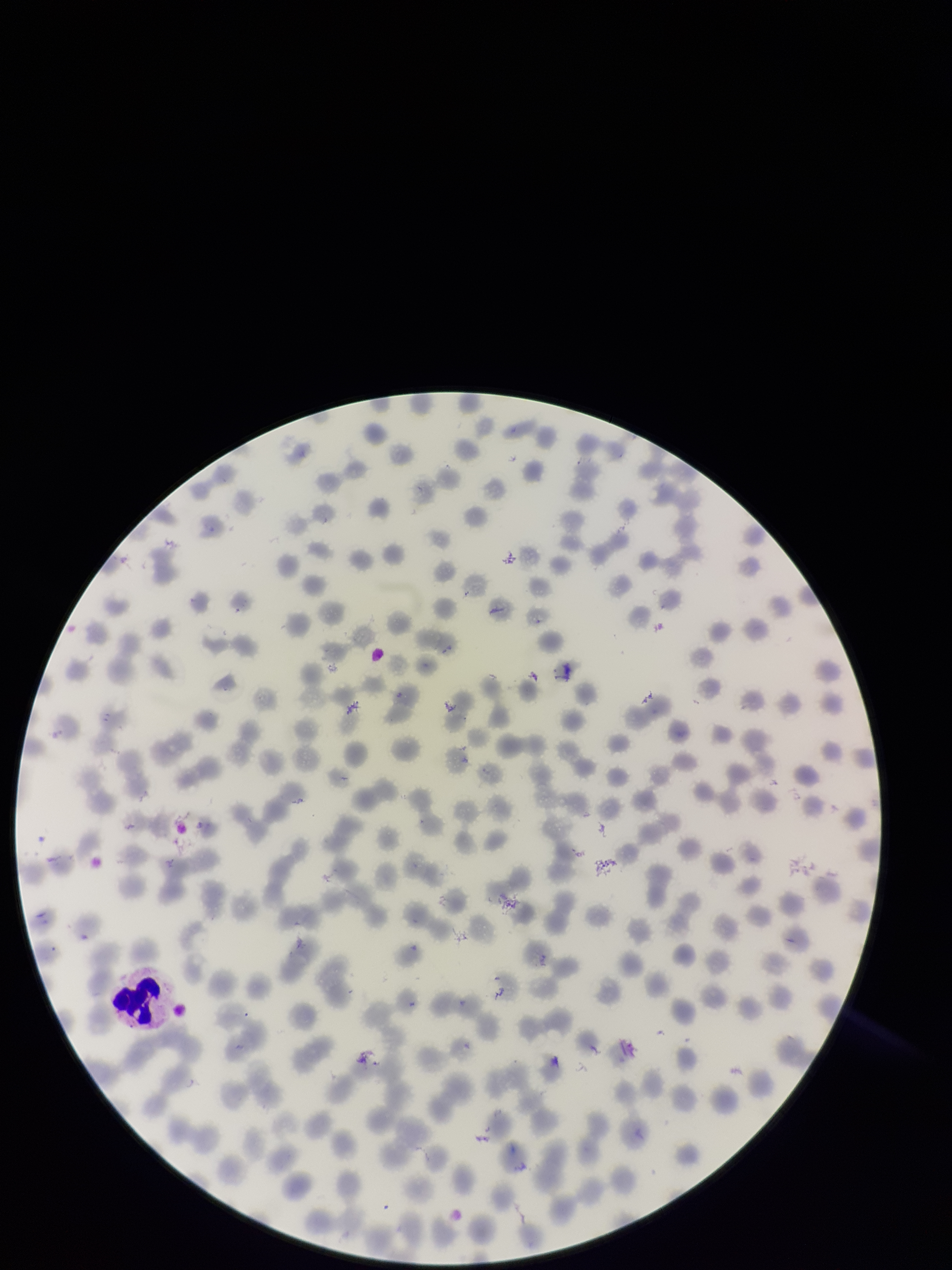 Stained with Giemsa. Red blood cell count: 225. Image is 952×1270 pixels. One field from this slide. Preparation: thin blood smear. Patient malaria status: positive. Smartphone photograph taken through the eyepiece of a microscope. Species reported for this patient: Plasmodium falciparum. Parasitized red blood cells: none detected. Parasitized red blood cell count: 0.